Assess this cell for malaria.
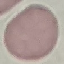

Uninfected.

Summary:
  - Stain: Giemsa
  - Image type: automatically extracted cell patch, resized to 64 × 64 pixels
  - Capture: smartphone through the microscope eyepiece
  - Preparation: thin blood smear